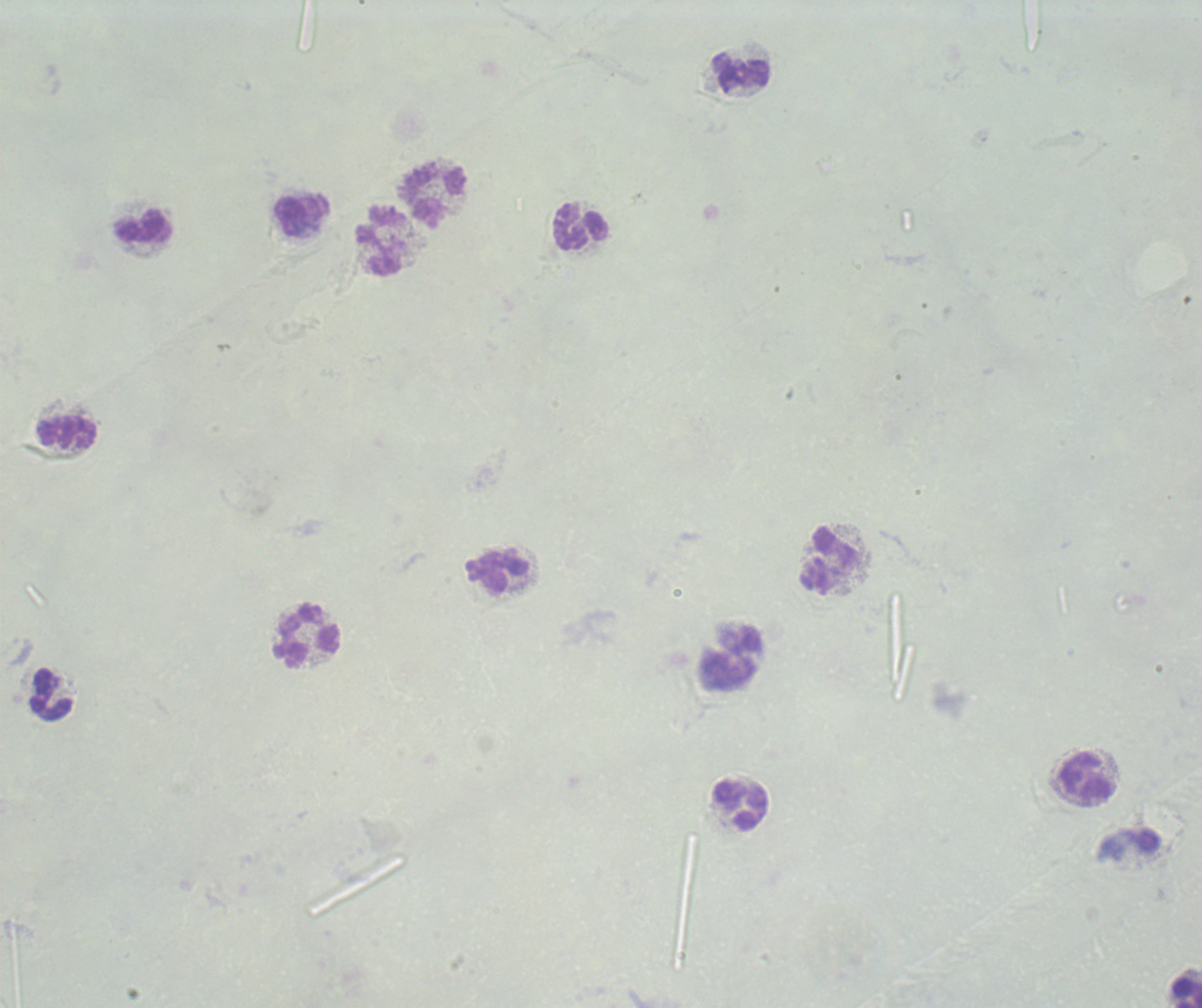

coordinate format = approximate centers as (x, y) in pixels
leukocyte locations = (741, 72), (433, 193), (303, 215), (580, 225), (143, 228), (379, 242), (68, 433), (829, 560), (497, 573), (307, 636), (51, 695), (1087, 777), (742, 806), (1188, 992)
image size = 1202×1008 pixels
stain = Romanowsky
context = previously used in an actual diagnosis
background quality = poor
preparation = thick blood smear
field of view = one from this slide
magnification = 100x
result = no malaria parasites seen